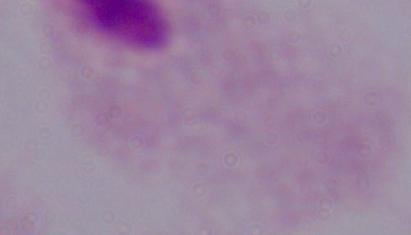
modality: micrograph
magnification: 1000x
identification: trichomonad